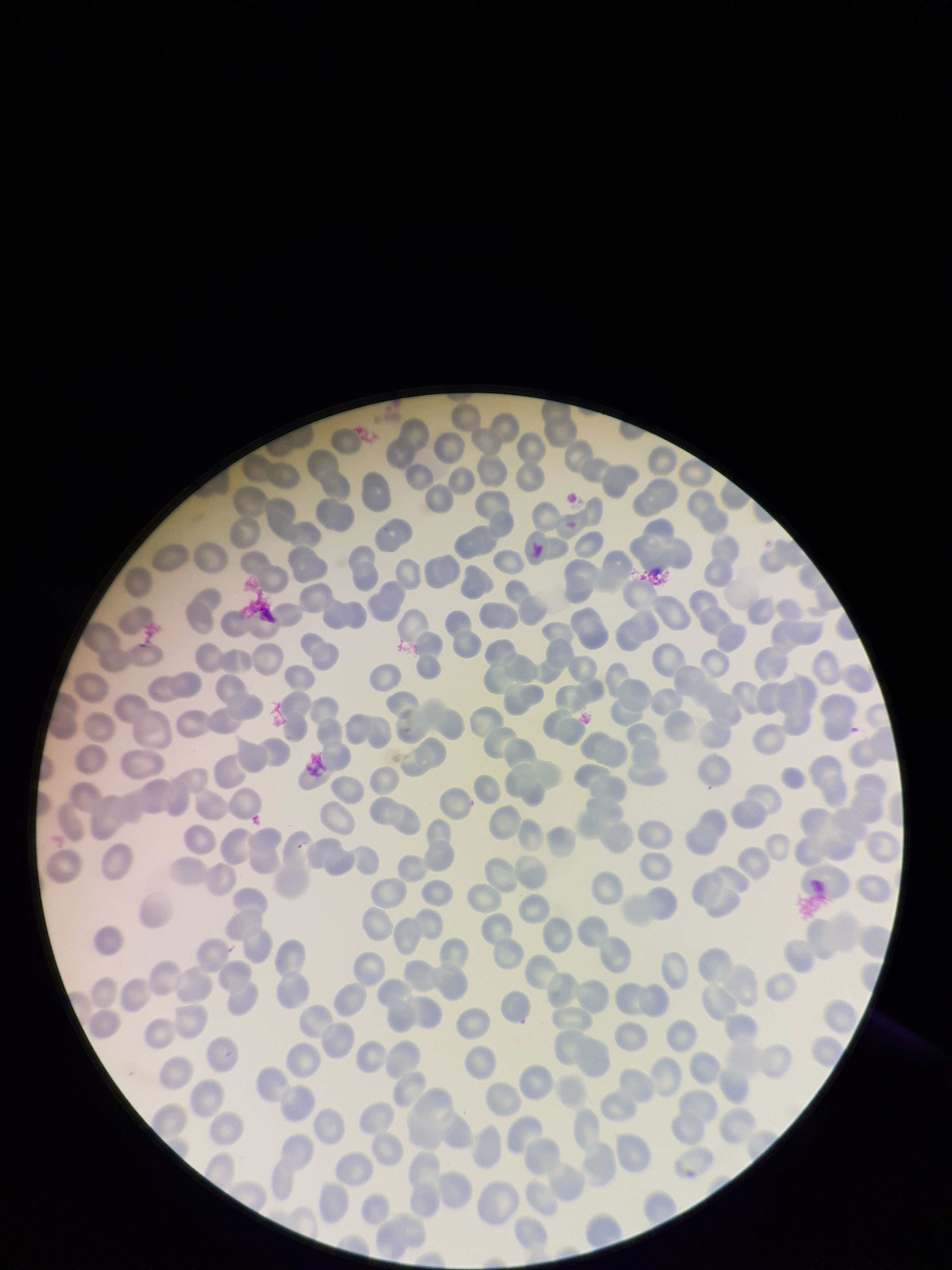

Summary:
  - Red blood cell count: 264
  - Patient malaria status: negative
  - Capture: smartphone photograph through the microscope eyepiece
  - Field of view: one from this slide
  - Image size: 952×1270 pixels
  - Preparation: thin
  - Parasitized red blood cells: none seen
  - Parasitized red blood cell count: 0
  - Stain: Giemsa